Report the malaria status of this cell.
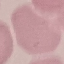

Uninfected.

Cell patch, automatically extracted from a larger field of view and resized to 64 × 64 pixels. Thin smear of blood. Giemsa-stained preparation. Photographed with a smartphone camera at the microscope eyepiece.